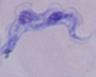
Summary:
  - Identification: trypanosome
  - Modality: photomicrograph
  - Magnification: 1000x